Name the cell type shown.
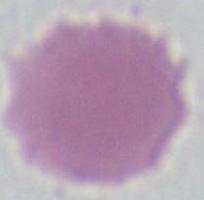
An erythrocyte.

Summary:
  - Magnification: 1000x
  - Modality: photomicrograph